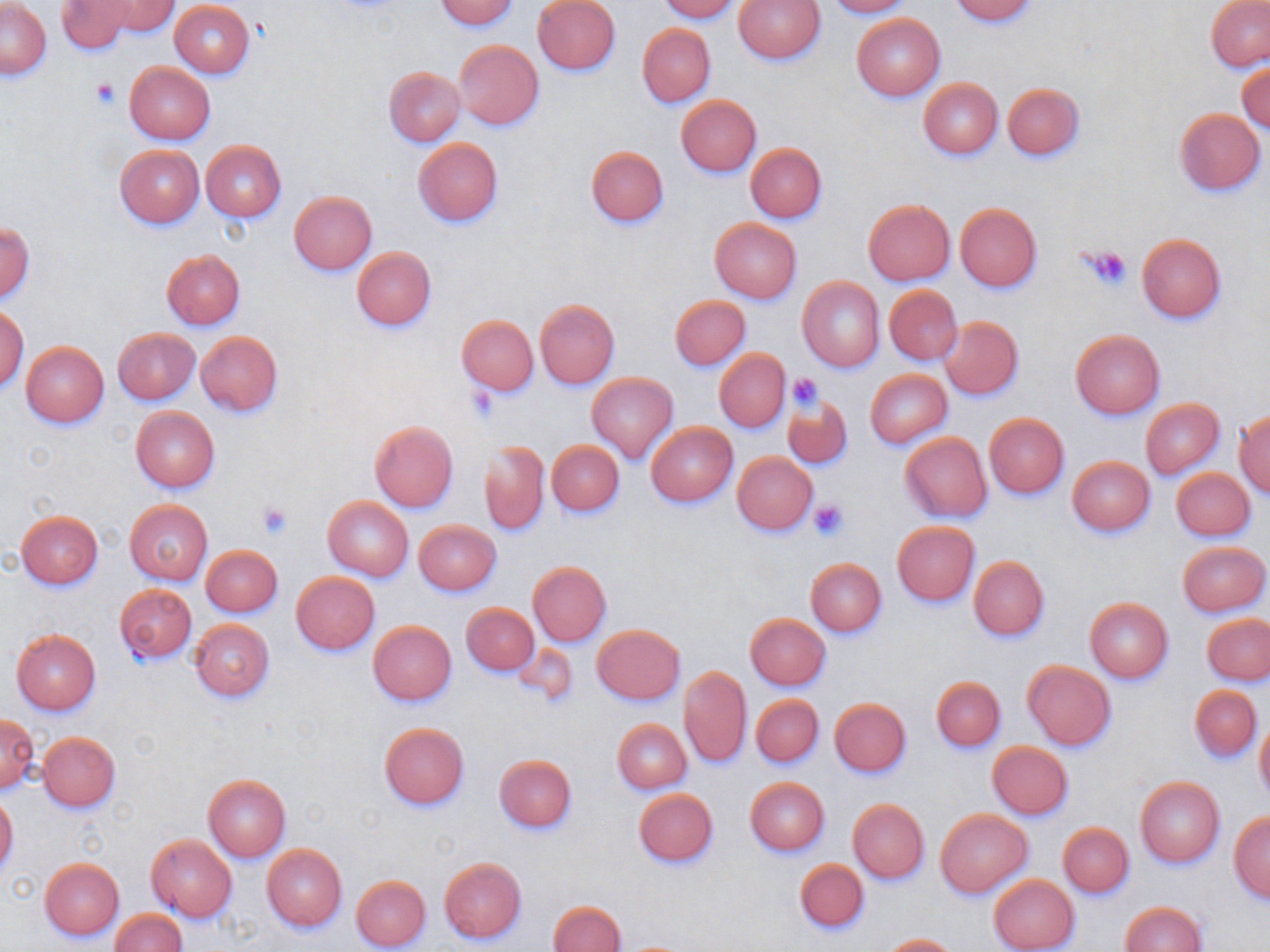 Approximate bounding boxes as [x1, y1, x2, y2] in pixels. Uninfected red blood cell locations: [91, 0, 178, 37], [437, 0, 518, 30], [660, 0, 739, 22], [734, 0, 826, 64], [822, 0, 911, 17], [948, 0, 1038, 24], [168, 1, 254, 78], [533, 1, 620, 74], [1207, 1, 1270, 71], [2, 2, 52, 79], [56, 2, 133, 53], [851, 13, 946, 101], [638, 24, 716, 106], [454, 40, 543, 130], [1237, 62, 1270, 135], [125, 63, 216, 144], [384, 67, 465, 147], [919, 78, 1003, 160], [1003, 83, 1084, 159], [676, 96, 761, 177], [1172, 108, 1266, 196], [412, 138, 503, 227], [200, 140, 287, 221], [745, 143, 827, 222], [116, 145, 205, 228], [586, 146, 669, 227], [289, 191, 378, 275], [863, 199, 955, 285], [955, 205, 1042, 292], [709, 218, 803, 303], [2, 222, 35, 301], [1136, 234, 1226, 323], [352, 246, 436, 332], [162, 250, 245, 329], [797, 277, 886, 372], [884, 285, 962, 365], [670, 294, 750, 371], [534, 300, 620, 388], [0, 305, 29, 391], [457, 315, 538, 395], [940, 316, 1023, 401], [113, 327, 199, 404], [1070, 330, 1165, 419], [195, 332, 284, 417], [21, 341, 108, 428], [715, 349, 790, 432], [865, 369, 953, 448], [587, 372, 677, 463], [782, 394, 854, 469], [1141, 399, 1224, 479], [130, 407, 220, 491], [1234, 410, 1270, 498], [984, 413, 1070, 499], [370, 421, 459, 512], [646, 421, 737, 507], [900, 433, 992, 521], [481, 440, 549, 535], [547, 440, 624, 516], [733, 452, 818, 535], [1067, 455, 1155, 536], [1171, 468, 1256, 540], [323, 497, 413, 580], [126, 499, 212, 584], [16, 511, 103, 591], [414, 519, 502, 596], [891, 521, 980, 606], [1176, 540, 1269, 616], [201, 544, 282, 616], [969, 556, 1050, 641], [806, 558, 887, 637], [528, 561, 611, 647], [291, 572, 380, 655], [115, 584, 196, 664], [1084, 597, 1175, 683], [462, 603, 539, 676], [1199, 611, 1267, 759], [745, 613, 832, 690], [1203, 613, 1270, 685], [189, 619, 275, 702], [369, 621, 456, 705], [593, 624, 685, 704], [11, 629, 101, 714], [1022, 661, 1116, 750], [678, 666, 751, 768], [931, 675, 1006, 752], [1190, 686, 1262, 761], [752, 695, 824, 767], [829, 699, 911, 777], [1, 714, 39, 792], [618, 716, 697, 866], [1255, 716, 1270, 805], [613, 719, 692, 794], [380, 722, 469, 810], [38, 731, 121, 812], [988, 742, 1074, 820], [494, 754, 577, 832], [203, 776, 291, 861], [745, 777, 831, 855], [1135, 777, 1225, 867], [635, 788, 718, 867], [0, 795, 19, 875], [848, 799, 929, 883], [936, 810, 1032, 897], [1228, 812, 1270, 903], [1058, 822, 1134, 897], [147, 834, 237, 922], [263, 844, 347, 931], [438, 855, 528, 945], [39, 858, 124, 941], [794, 858, 870, 934], [351, 874, 432, 951], [989, 874, 1080, 952], [548, 901, 626, 952], [1120, 902, 1208, 951], [111, 908, 186, 952], [882, 933, 958, 951]. Platelet locations: [92, 78, 119, 107], [1080, 243, 1136, 291], [787, 374, 823, 412], [467, 385, 499, 423], [808, 497, 850, 540], [257, 501, 292, 539]. Slide-level diagnosis: no evidence of blood parasites. Light microscopy. One field of a larger specimen. Image is 1270×952 pixels. May-Grünwald-Giemsa-stained preparation. Captured at 1000x magnification. Thin blood smear.